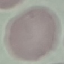

Result: negative for malaria parasites. Giemsa-stained preparation. Automatically extracted cell patch, resized to 64 × 64 pixels. Thin blood film. Photographed with a smartphone camera at the microscope eyepiece.